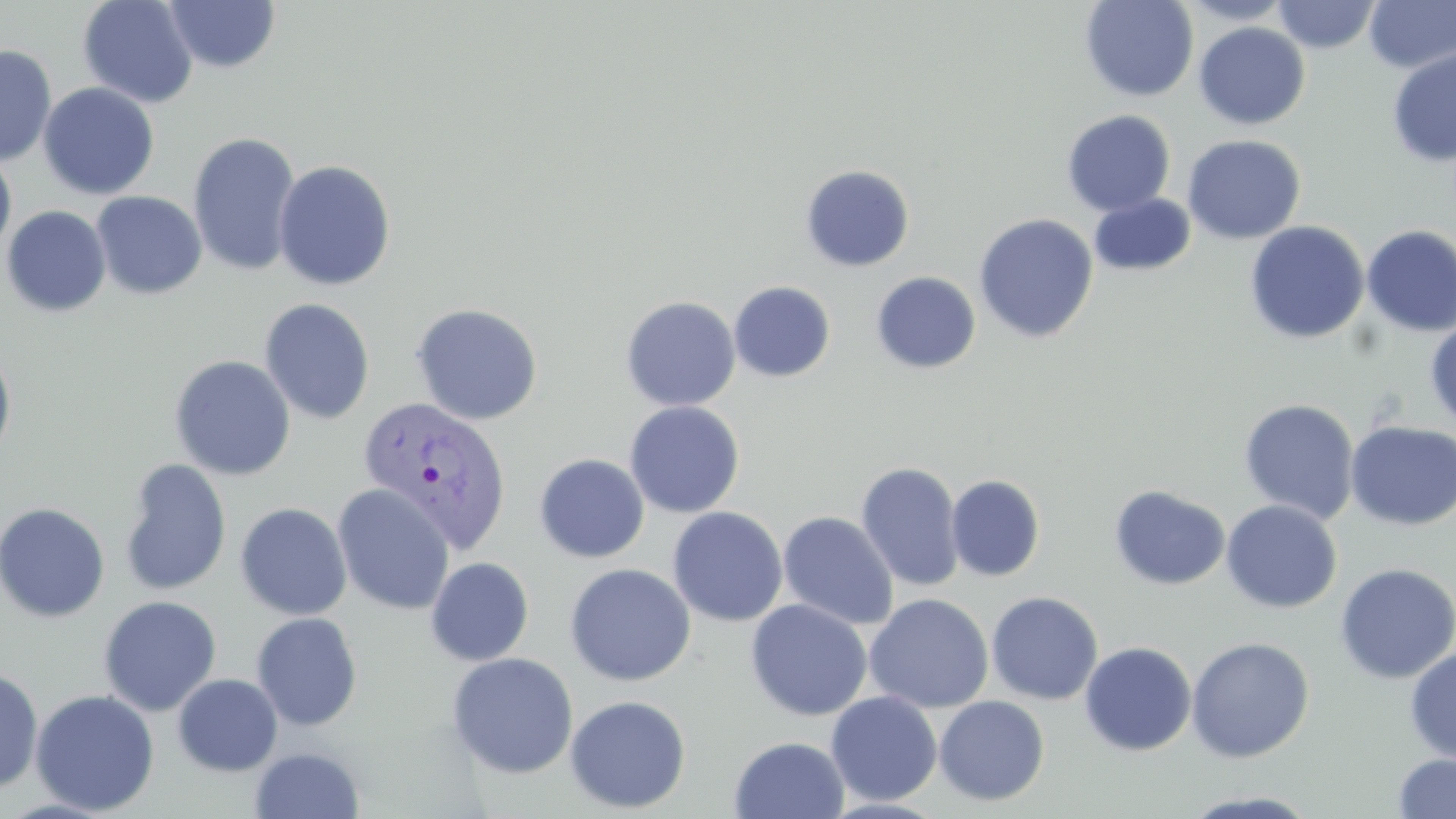

Approximate bounding boxes as [x1, y1, x2, y2] in pixels. Uninfected red blood cell locations: [77, 0, 199, 108], [1079, 0, 1199, 102], [1177, 0, 1294, 25], [1272, 0, 1380, 53], [1364, 0, 1456, 73], [163, 1, 281, 74], [1081, 12, 1313, 110], [1193, 22, 1310, 130], [0, 44, 57, 167], [1387, 48, 1456, 167], [38, 82, 160, 200], [1061, 110, 1175, 216], [187, 131, 302, 278], [1182, 134, 1306, 244], [0, 147, 17, 258], [273, 159, 396, 291], [800, 165, 915, 271], [91, 191, 207, 300], [1089, 193, 1196, 276], [1, 205, 112, 317], [974, 213, 1098, 344], [1245, 221, 1369, 344], [1361, 225, 1456, 338], [870, 271, 981, 374], [728, 281, 836, 382], [620, 296, 740, 411], [258, 298, 376, 425], [410, 302, 544, 425], [1425, 319, 1456, 429], [0, 344, 17, 469], [169, 355, 296, 481], [1238, 399, 1360, 524], [624, 401, 745, 517], [1346, 420, 1456, 531], [533, 453, 649, 563], [118, 458, 232, 597], [855, 461, 965, 592], [946, 474, 1045, 581], [332, 484, 455, 615], [1109, 484, 1231, 591], [1221, 500, 1342, 613], [0, 501, 110, 623], [235, 502, 352, 621], [667, 506, 788, 627], [778, 511, 900, 631], [425, 556, 534, 666], [1334, 562, 1456, 685], [564, 563, 696, 686], [986, 591, 1103, 705], [864, 593, 993, 713], [98, 595, 222, 716], [745, 599, 872, 721], [251, 612, 363, 731], [1186, 636, 1315, 763], [1079, 641, 1197, 756], [1405, 645, 1456, 765], [446, 652, 579, 779], [0, 665, 44, 794], [172, 673, 283, 777], [29, 690, 159, 815], [826, 690, 942, 806], [564, 694, 691, 814], [934, 695, 1049, 806], [729, 735, 849, 819], [249, 747, 366, 818], [1392, 753, 1456, 818], [1179, 790, 1321, 818]. Plasmodium vivax-infected red blood cell locations: [357, 395, 512, 554]. Slide-level diagnosis: Plasmodium vivax. 1000x magnification. One field of a larger specimen. Image is 1456×819 pixels. May-Grünwald-Giemsa stain. Thin blood smear. Light microscopy.